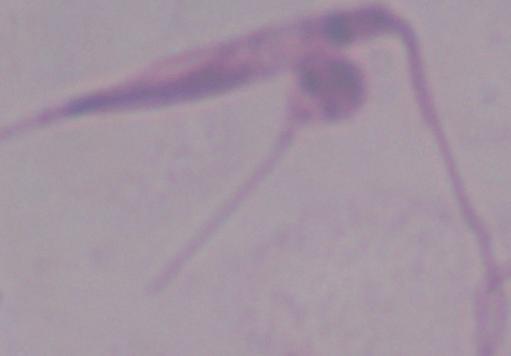
Summary:
  - Identification: Leishmania
  - Modality: photomicrograph
  - Magnification: 1000x